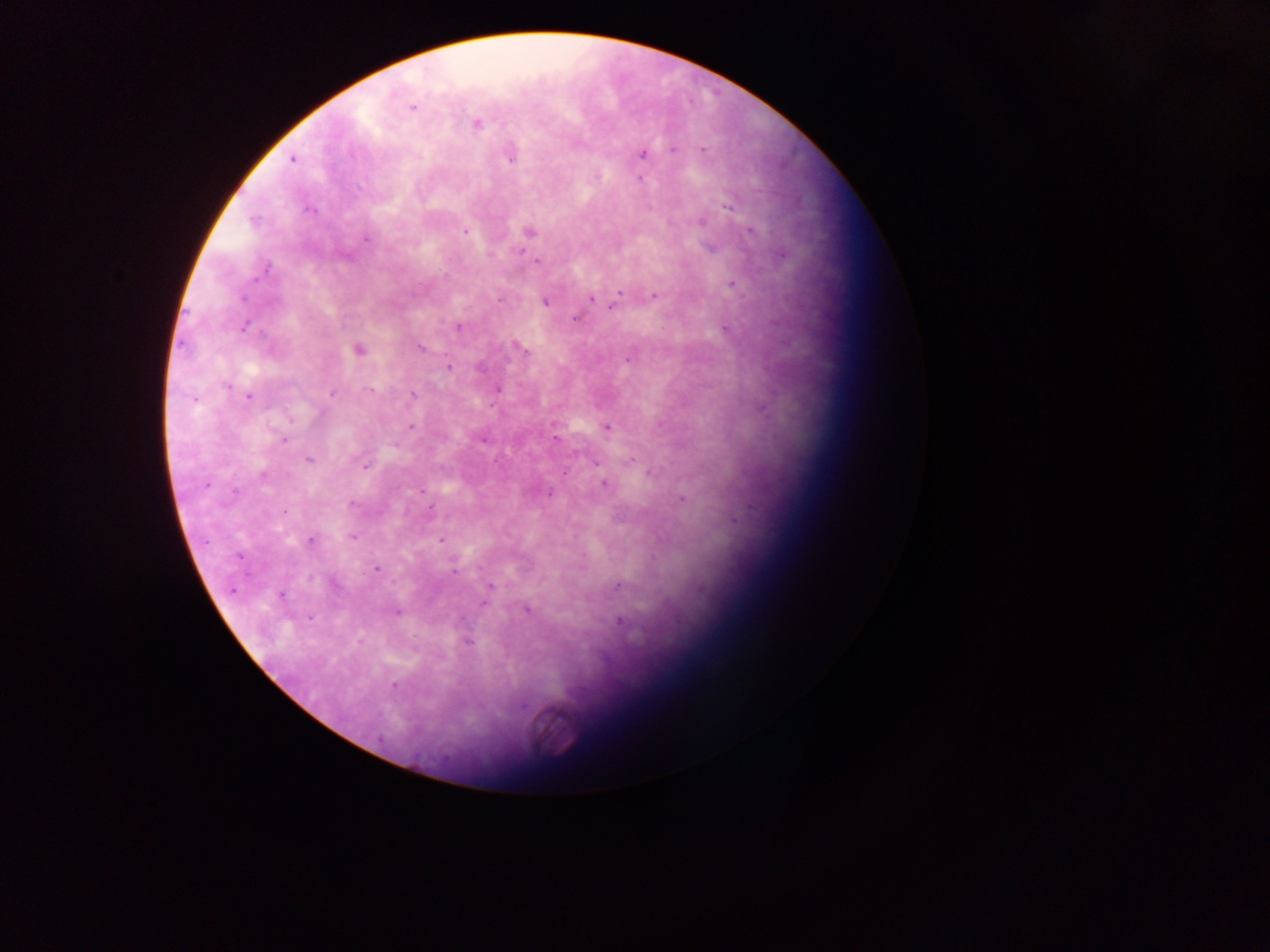
capture: mobile-phone photograph through a microscope
image_size: 1270×952 pixels
preparation: thick blood film
field_of_view: single
plasmodium_parasite_locations: 'approximate centers as [x, y] in pixels: [412, 108], [477, 124], [672, 149], [702, 150], [642, 154], [292, 159], [510, 159], [598, 177], [639, 178], [727, 206], [310, 209], [253, 220], [702, 222], [466, 231], [529, 231], [750, 231], [366, 239], [521, 251], [782, 254], [346, 255], [536, 261], [266, 269], [732, 284], [619, 292], [654, 295], [242, 298], [590, 299], [499, 300], [545, 302], [597, 302], [611, 306], [574, 318], [459, 326], [244, 327], [725, 329], [420, 348], [521, 349], [359, 350], [628, 358], [449, 366], [226, 386], [370, 389], [497, 390], [332, 394], [412, 395], [249, 397], [192, 399], [491, 407], [411, 427], [606, 428], [555, 438], [284, 440], [482, 440], [394, 445], [307, 459], [631, 460], [495, 461], [365, 467], [565, 472], [650, 473], [262, 476], [604, 484], [207, 485], [422, 491], [235, 492], [550, 494], [683, 499], [351, 504], [283, 513], [733, 521], [353, 537], [310, 540], [441, 540], [238, 557], [377, 569], [455, 572], [618, 585], [490, 586], [232, 590], [281, 595], [484, 603], [526, 610], [397, 612], [311, 618], [620, 621], [468, 642], [395, 686], [381, 739]'
country: Ghana